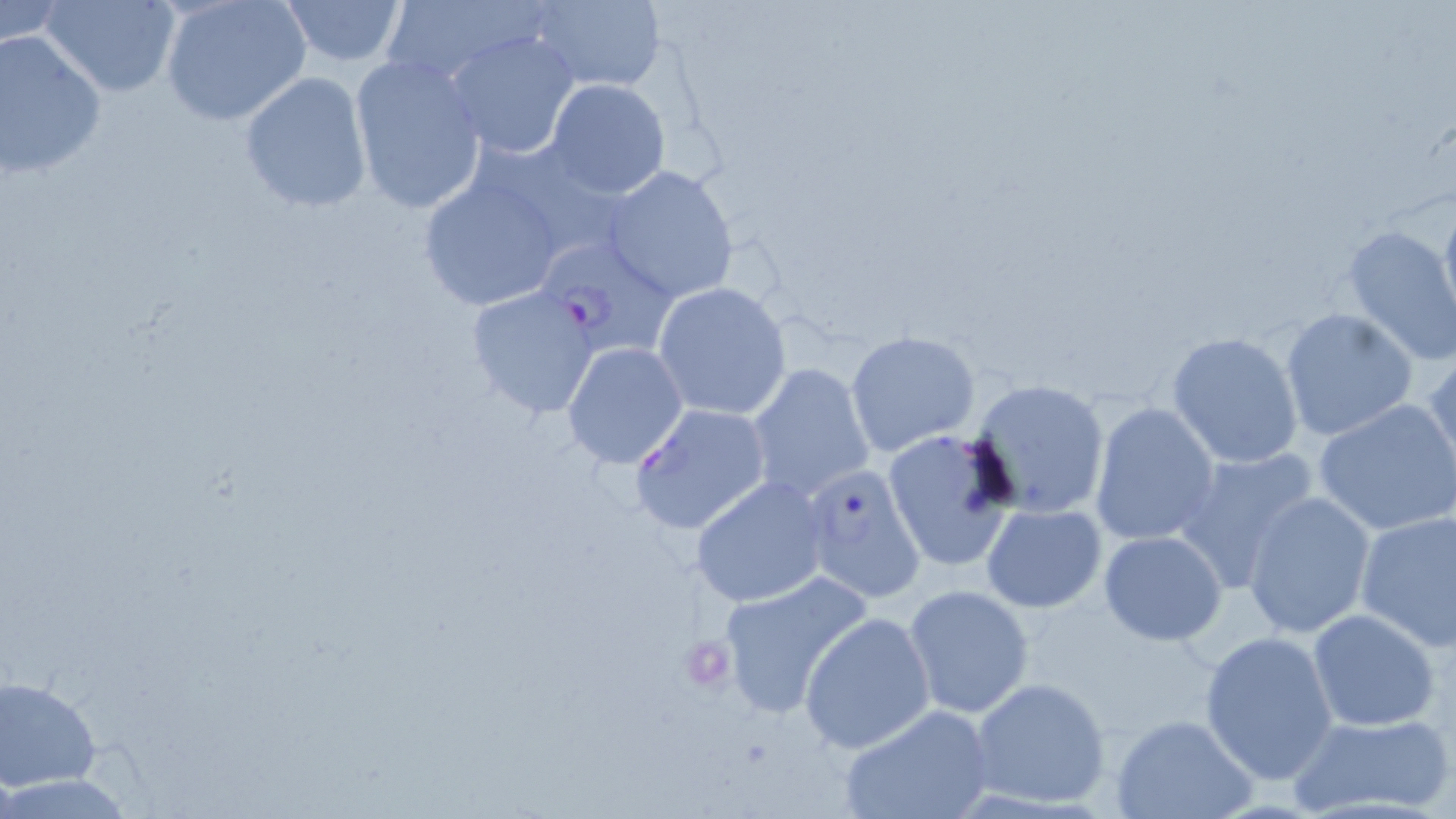

slide-level diagnosis = Plasmodium falciparum
magnification = 1000x
Plasmodium falciparum-infected red blood cell locations = approximate bounding boxes as [x1, y1, x2, y2] in pixels: [534, 231, 682, 357], [628, 403, 773, 537], [800, 463, 926, 604]
image size = 1456×819 pixels
preparation = thin blood film
field of view = one of a larger specimen
platelet locations = approximate bounding boxes as [x1, y1, x2, y2] in pixels: [682, 636, 734, 690]
stain = May-Grünwald-Giemsa
modality = optical microscopy
uninfected red blood cell locations = approximate bounding boxes as [x1, y1, x2, y2] in pixels: [38, 0, 182, 98], [278, 0, 407, 67], [377, 0, 541, 91], [0, 1, 69, 50], [157, 1, 311, 126], [527, 1, 667, 91], [443, 28, 581, 160], [0, 31, 108, 180], [349, 54, 488, 214], [238, 70, 375, 213], [545, 78, 671, 201], [413, 164, 575, 313], [601, 164, 740, 306], [1437, 193, 1456, 336], [1339, 224, 1456, 365], [653, 281, 792, 421], [465, 286, 603, 418], [1278, 307, 1417, 439], [846, 329, 980, 457], [1167, 332, 1306, 469], [561, 341, 689, 468], [1426, 351, 1456, 483], [746, 363, 875, 505], [968, 378, 1111, 519], [1314, 400, 1456, 536], [1089, 402, 1220, 546], [882, 429, 1017, 572], [1171, 447, 1318, 589], [691, 475, 829, 607], [1241, 490, 1376, 639], [982, 504, 1106, 614], [1354, 510, 1456, 655], [1098, 530, 1227, 645], [717, 570, 874, 719], [904, 585, 1036, 721], [1307, 609, 1440, 731], [800, 613, 934, 756], [1199, 631, 1339, 784], [1, 676, 102, 792], [969, 676, 1111, 808], [838, 702, 995, 819], [1286, 712, 1455, 817], [1110, 714, 1256, 819]